Give the position of every malaria parasite.
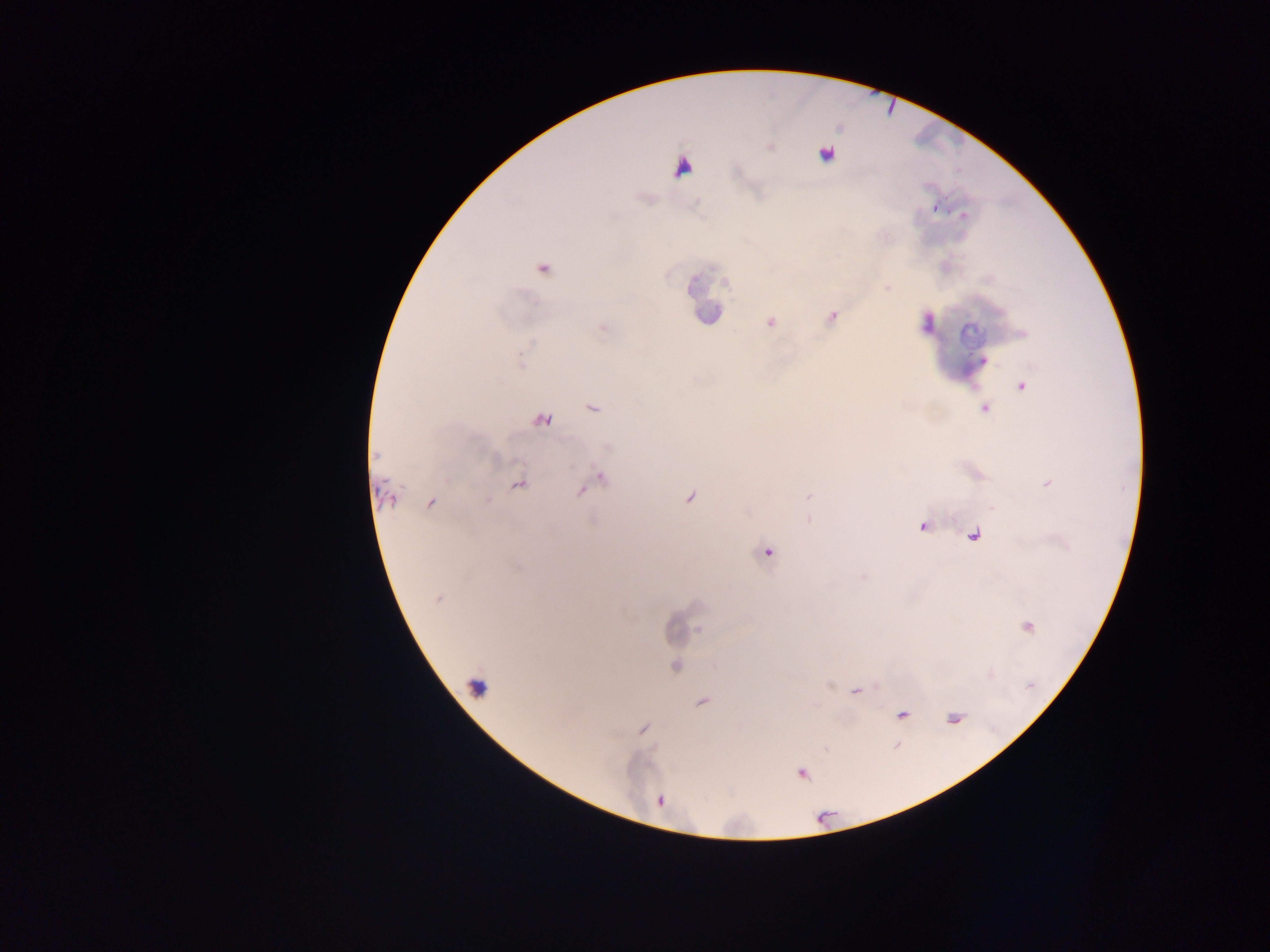
Approximate centers as [x, y] in pixels.
Malaria parasites: [935, 207], [964, 215], [542, 270], [887, 289], [770, 323], [983, 360], [1021, 386], [592, 408], [984, 408], [542, 420], [519, 484], [387, 496], [487, 500], [430, 502], [922, 527], [973, 536], [767, 553], [437, 599], [1029, 627], [676, 665], [857, 692], [703, 703], [902, 715], [644, 729], [802, 773].

capture: mobile-phone photograph through a microscope
field_of_view: single
leukocyte_locations: 'approximate centers as [x, y] in pixels: [827, 154], [682, 162], [478, 685]'
country: Ghana
preparation: thick blood film
image_size: 1270×952 pixels